Classify this cell by malaria status.
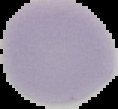
Uninfected.

Cell region segmented out of the field of view; the surrounding area is masked to black. Image is 118×109 pixels. From a thin blood film.